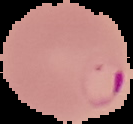
image_size: 133×124 pixels
image_type: segmented cell region on a black background
result: Plasmodium parasites identified
preparation: thin blood film